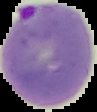
Cell region segmented out of the field of view; the surrounding area is masked to black. From a thin blood smear. Image is 97×112 pixels. Malaria status: parasitized.